State which parasite is depicted.
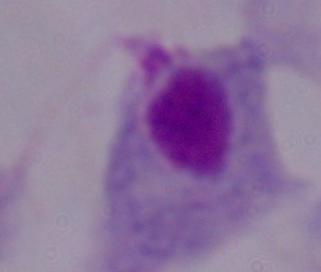

This is a trichomonad.

Photomicrograph. 1000x magnification.